Locate every Plasmodium falciparum-infected red blood cell.
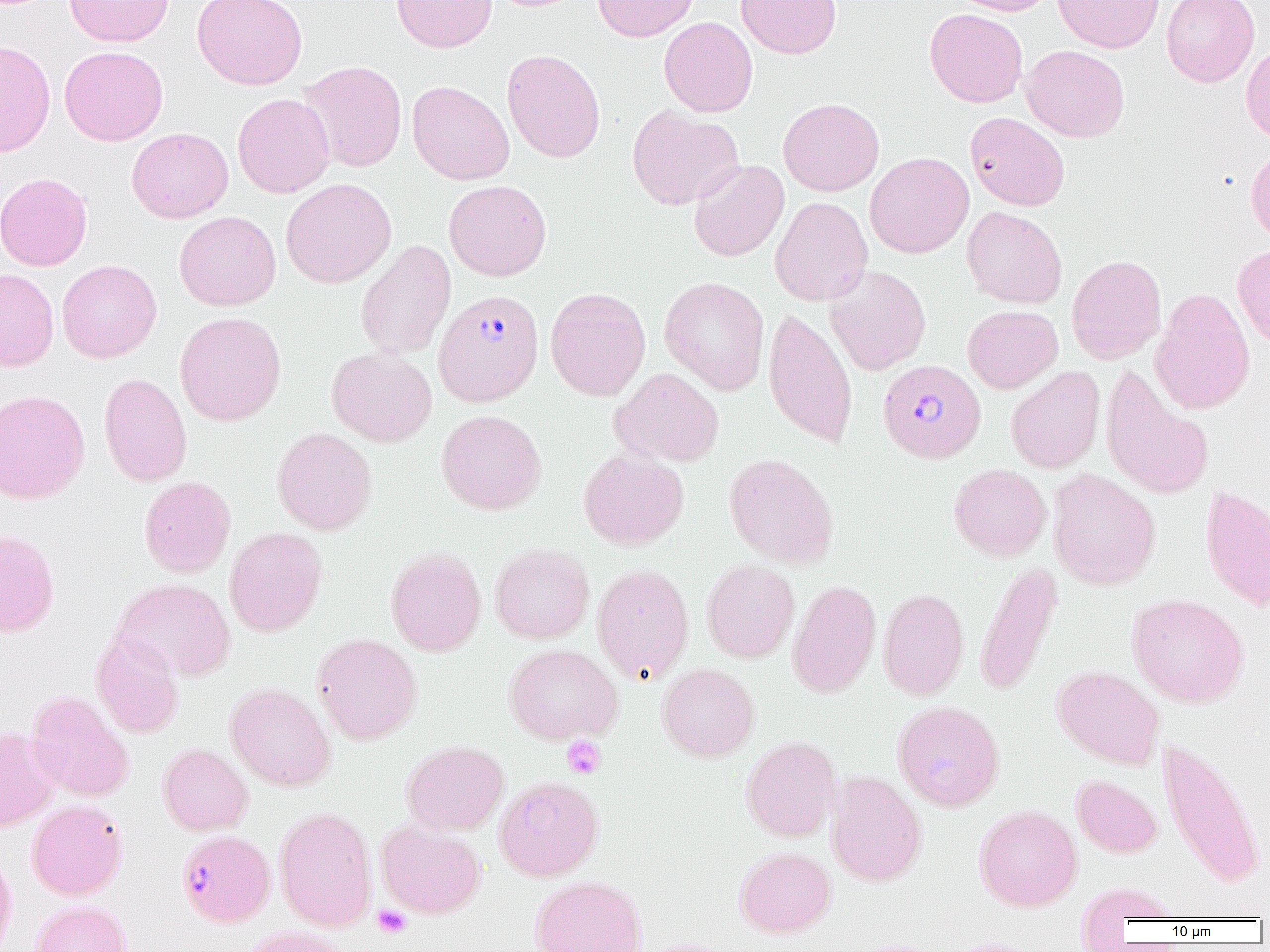

Approximate bounding boxes as [x1, y1, x2, y2] in pixels.
Plasmodium falciparum-infected red blood cells: [433, 290, 544, 406], [878, 359, 986, 463], [177, 830, 276, 927].

slide_level_diagnosis: Plasmodium falciparum
field_of_view: single
modality: optical microscopy
preparation: thin blood smear
uninfected_red_blood_cell_locations: 'approximate bounding boxes as [x1, y1, x2, y2] in pixels: [64, 0, 173, 47], [193, 0, 307, 90], [391, 0, 496, 53], [486, 0, 587, 12], [593, 0, 699, 42], [736, 0, 842, 58], [950, 0, 1056, 16], [1053, 0, 1164, 53], [1162, 0, 1260, 87], [925, 8, 1028, 107], [659, 16, 758, 117], [1241, 39, 1270, 144], [0, 40, 56, 157], [59, 45, 168, 146], [1021, 45, 1130, 142], [502, 49, 605, 162], [299, 61, 407, 172], [407, 80, 514, 185], [232, 93, 335, 198], [778, 97, 884, 196], [627, 104, 744, 210], [965, 112, 1070, 211], [126, 128, 233, 223], [1246, 146, 1270, 244], [865, 152, 974, 258], [688, 159, 789, 262], [0, 172, 93, 271], [281, 178, 396, 288], [444, 180, 552, 281], [770, 196, 873, 306], [962, 207, 1067, 309], [174, 211, 281, 311], [355, 240, 456, 360], [1233, 244, 1270, 352], [1066, 254, 1167, 365], [57, 260, 162, 362], [825, 266, 931, 375], [0, 268, 59, 372], [659, 276, 770, 395], [545, 287, 651, 401], [1150, 288, 1255, 415], [962, 305, 1063, 393], [763, 307, 858, 449], [174, 312, 286, 426], [327, 348, 436, 447], [1006, 366, 1105, 474], [1100, 367, 1215, 500], [610, 368, 724, 468], [99, 373, 192, 487], [0, 389, 90, 504], [436, 409, 546, 515], [272, 427, 377, 535], [578, 447, 689, 550], [724, 453, 838, 569], [949, 463, 1052, 561], [1048, 469, 1161, 590], [139, 476, 236, 578], [1200, 484, 1270, 611], [224, 527, 328, 637], [0, 530, 59, 637], [490, 544, 594, 643], [386, 547, 486, 656], [702, 559, 799, 663], [974, 561, 1062, 697], [592, 563, 694, 684], [113, 578, 235, 682], [787, 579, 881, 699], [878, 587, 968, 700], [1128, 593, 1249, 707], [91, 631, 184, 738], [312, 633, 422, 745], [504, 643, 623, 744], [657, 663, 759, 762], [1052, 665, 1165, 769], [225, 683, 336, 791], [25, 690, 134, 802], [892, 700, 1004, 811], [0, 728, 61, 832], [741, 736, 841, 842], [1158, 737, 1265, 889], [402, 740, 509, 835], [158, 743, 253, 836], [825, 771, 927, 887], [1072, 775, 1162, 858], [494, 776, 604, 881], [27, 800, 127, 900], [974, 804, 1082, 911], [275, 807, 376, 932], [376, 820, 485, 919], [735, 846, 836, 938], [0, 849, 17, 952], [530, 875, 648, 952], [1077, 882, 1181, 931], [30, 900, 132, 952], [241, 926, 353, 952], [634, 938, 741, 952]'
image_size: 1270×952 pixels
magnification: 1000x
platelet_locations: 'approximate bounding boxes as [x1, y1, x2, y2] in pixels: [562, 736, 606, 779], [373, 905, 411, 938]'